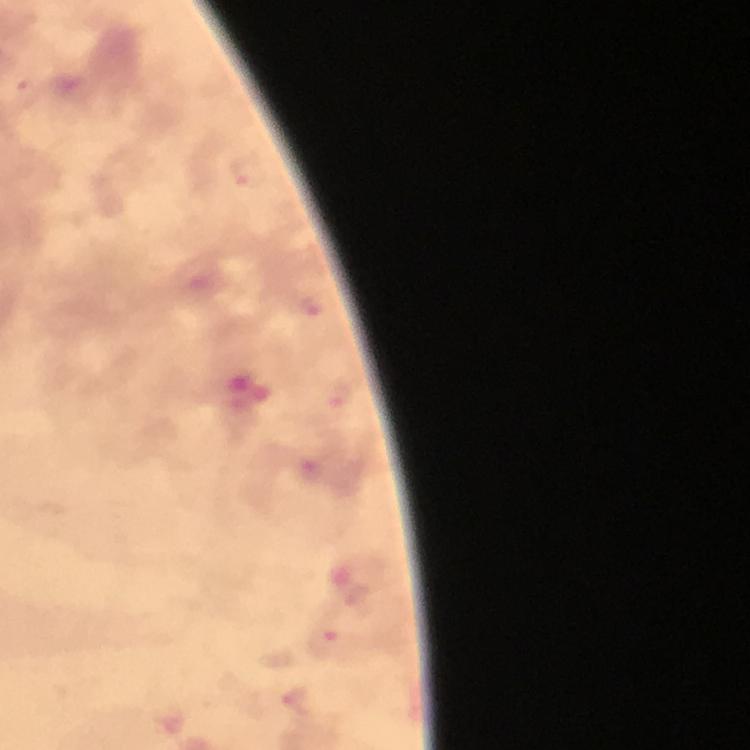

Approximate object centers, in pixels from the top-left corner. Plasmodium parasite locations: (x=248, y=172), (x=312, y=306), (x=337, y=396), (x=326, y=642), (x=295, y=702). From a diagnostic examination for malaria. Immersion oil applied. Smartphone photograph taken through a microscope. Image is 750×750 pixels. 100x magnification. A crop from one field of view. Thick smear. Giemsa stain.